Report the malaria status of this cell.
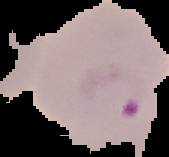
Parasitized.

Summary:
  - Image size: 169×157 pixels
  - Preparation: thin blood film
  - Image type: segmented cell region with the area outside set to black